Report the malaria status of this cell.
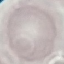

Uninfected.

Giemsa-stained preparation. Acquired by smartphone through the microscope eyepiece. Thin blood smear. Automatically extracted cell patch, resized to 64 × 64 pixels.